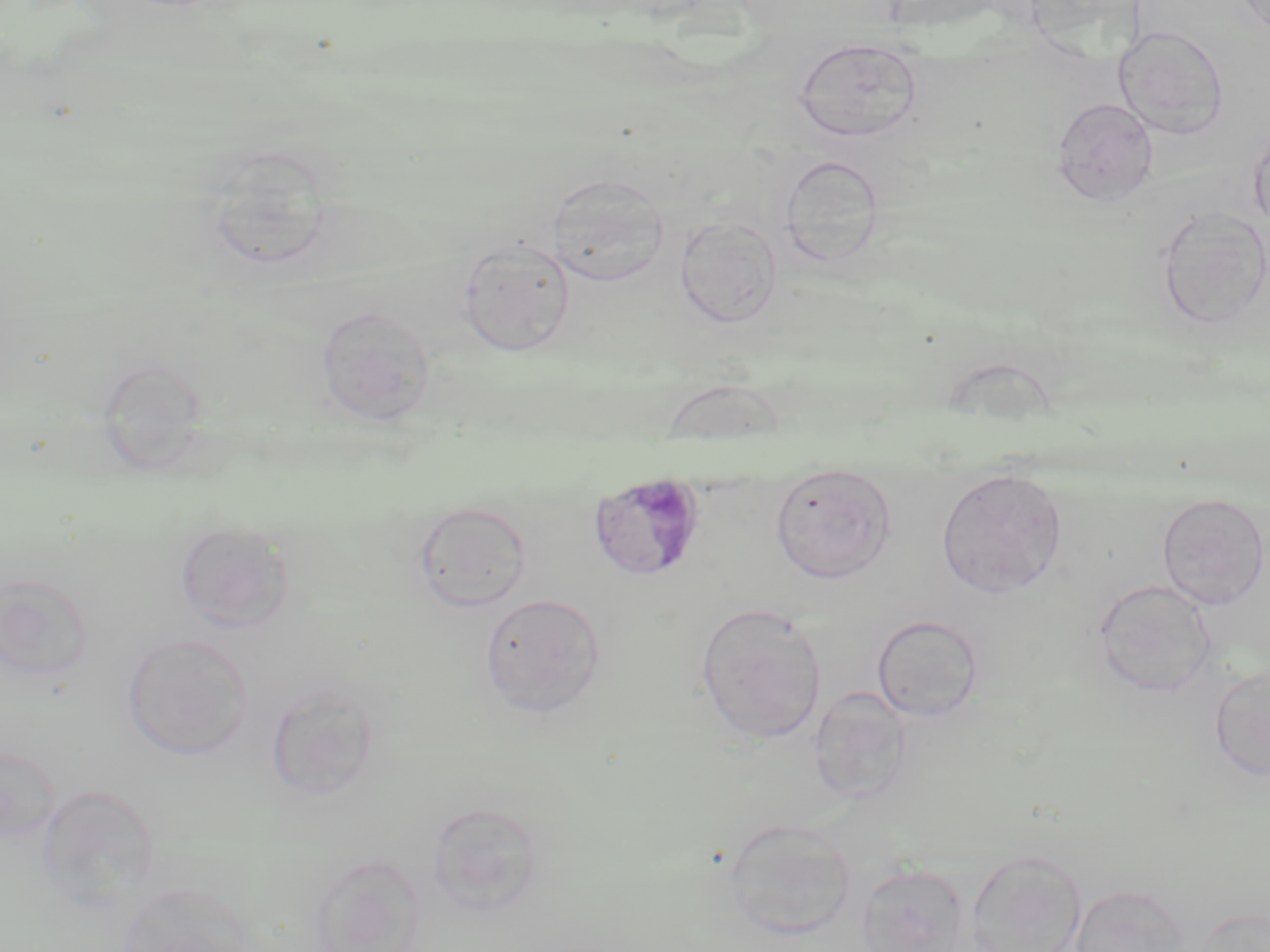

Summary:
  - Coordinate format: approximate bounding boxes as named x1/y1/x2/y2 corners in pixels
  - Plasmodium malariae-infected red blood cell locations: (x1=588, y1=471, x2=708, y2=582)
  - Uninfected red blood cell locations: (x1=1113, y1=25, x2=1230, y2=140), (x1=793, y1=37, x2=924, y2=143), (x1=1052, y1=97, x2=1158, y2=207), (x1=1249, y1=126, x2=1270, y2=234), (x1=200, y1=145, x2=335, y2=273), (x1=780, y1=154, x2=884, y2=269), (x1=546, y1=174, x2=669, y2=286), (x1=1156, y1=207, x2=1269, y2=330), (x1=675, y1=216, x2=782, y2=327), (x1=457, y1=238, x2=575, y2=355), (x1=315, y1=304, x2=436, y2=425), (x1=770, y1=464, x2=897, y2=583), (x1=936, y1=468, x2=1068, y2=598), (x1=1156, y1=493, x2=1269, y2=610), (x1=414, y1=501, x2=532, y2=613), (x1=174, y1=520, x2=295, y2=632), (x1=0, y1=574, x2=95, y2=684), (x1=1093, y1=578, x2=1217, y2=698), (x1=479, y1=592, x2=606, y2=718), (x1=695, y1=603, x2=827, y2=745), (x1=872, y1=615, x2=984, y2=721), (x1=123, y1=633, x2=253, y2=760), (x1=1209, y1=666, x2=1270, y2=782), (x1=264, y1=680, x2=383, y2=803), (x1=809, y1=687, x2=914, y2=806), (x1=0, y1=741, x2=60, y2=845), (x1=36, y1=784, x2=160, y2=914), (x1=425, y1=801, x2=547, y2=917), (x1=723, y1=819, x2=857, y2=940), (x1=965, y1=849, x2=1088, y2=952), (x1=309, y1=853, x2=425, y2=952), (x1=857, y1=864, x2=971, y2=952), (x1=115, y1=882, x2=256, y2=952), (x1=1068, y1=883, x2=1191, y2=952), (x1=1189, y1=906, x2=1269, y2=952)
  - Slide-level diagnosis: Plasmodium malariae
  - Stain: May-Grünwald-Giemsa
  - Image size: 1270×952 pixels
  - Modality: optical microscopy
  - Preparation: thin blood film
  - Field of view: single
  - Magnification: 1000x